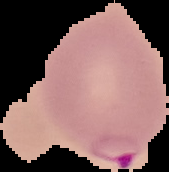

Summary:
  - Image size: 169×172 pixels
  - Preparation: thin blood smear
  - Image type: segmented cell region with the area outside set to black
  - Result: malaria parasites identified